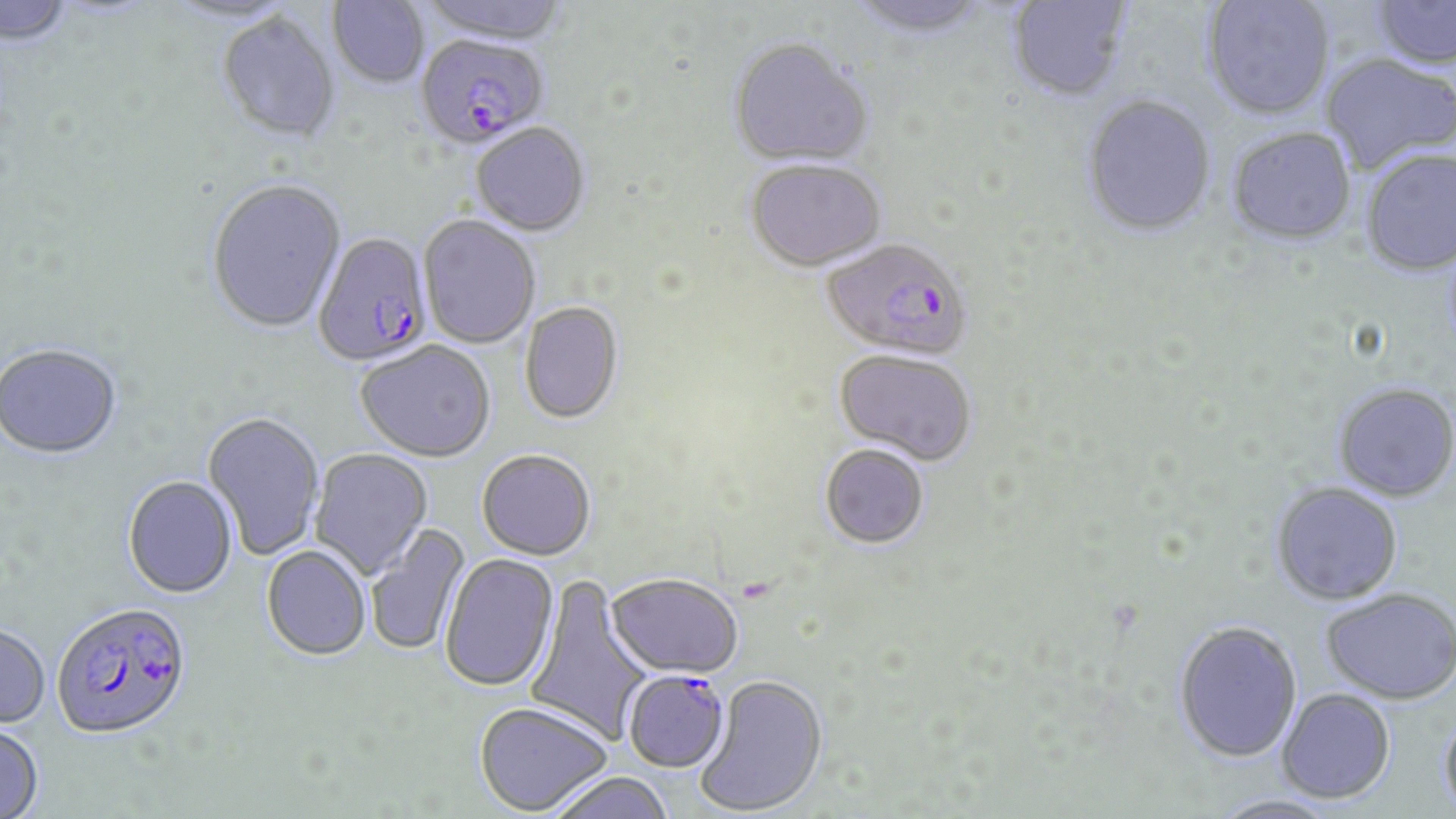
Summary:
  - Coordinate format: approximate bounding boxes as (x1, y1, x2, y2) in pixels
  - Plasmodium falciparum-infected red blood cell locations: (416, 37, 549, 152), (313, 235, 434, 368), (820, 240, 974, 364), (52, 604, 192, 741), (622, 671, 731, 774)
  - Uninfected red blood cell locations: (418, 0, 571, 47), (1007, 0, 1132, 104), (1374, 0, 1456, 72), (0, 1, 77, 51), (327, 1, 430, 91), (845, 1, 994, 43), (1202, 1, 1335, 121), (215, 14, 342, 146), (727, 40, 874, 171), (1320, 54, 1456, 175), (1081, 96, 1216, 239), (471, 125, 591, 238), (1227, 129, 1356, 248), (1361, 149, 1456, 277), (745, 162, 886, 274), (206, 180, 347, 335), (418, 216, 540, 349), (519, 303, 624, 426), (356, 342, 496, 464), (0, 346, 122, 461), (833, 351, 976, 467), (1332, 383, 1456, 502), (202, 413, 325, 561), (819, 445, 929, 550), (309, 449, 433, 579), (477, 451, 596, 562), (123, 477, 238, 600), (1271, 482, 1403, 606), (366, 523, 471, 656), (262, 546, 371, 661), (440, 553, 559, 692), (605, 575, 744, 680), (524, 576, 654, 746), (1321, 587, 1456, 705), (1172, 620, 1303, 763), (0, 626, 50, 730), (694, 674, 829, 816), (1277, 688, 1395, 804), (474, 702, 612, 815), (1438, 709, 1456, 817), (0, 721, 44, 818), (543, 772, 677, 819)
  - Slide-level diagnosis: Plasmodium falciparum
  - Modality: light microscopy
  - Field of view: one of a larger specimen
  - Image size: 1456×819 pixels
  - Stain: May-Grünwald-Giemsa
  - Preparation: thin blood film
  - Magnification: 1000x